State which cell type is depicted.
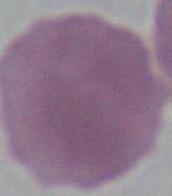
An erythrocyte.

Photomicrograph. 1000x magnification.